Describe the morphology of the erythrocytes.
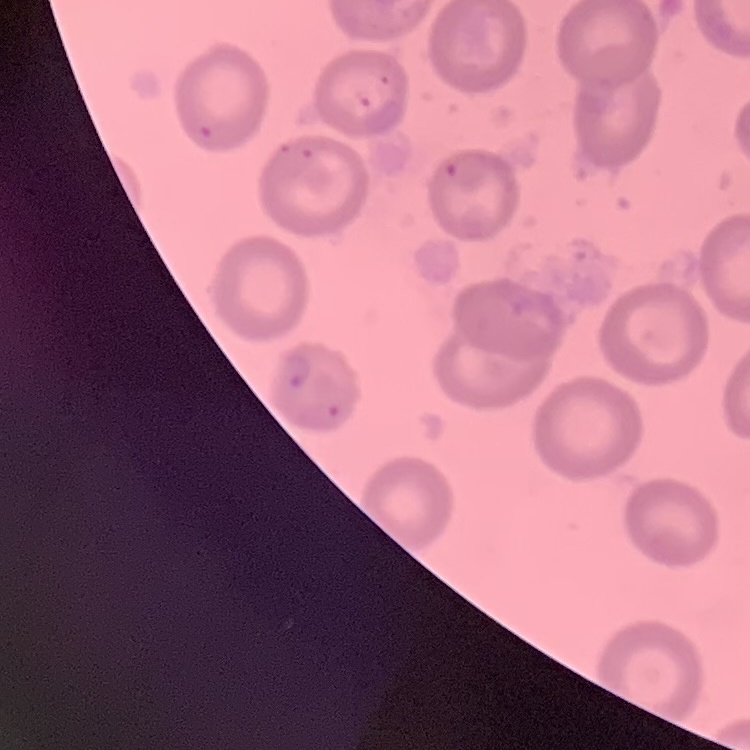
No rouleaux formation.

image type = square crop of a larger photomicrograph
stain = Field's or Giemsa
preparation = thin blood smear